Point out each Plasmodium parasite.
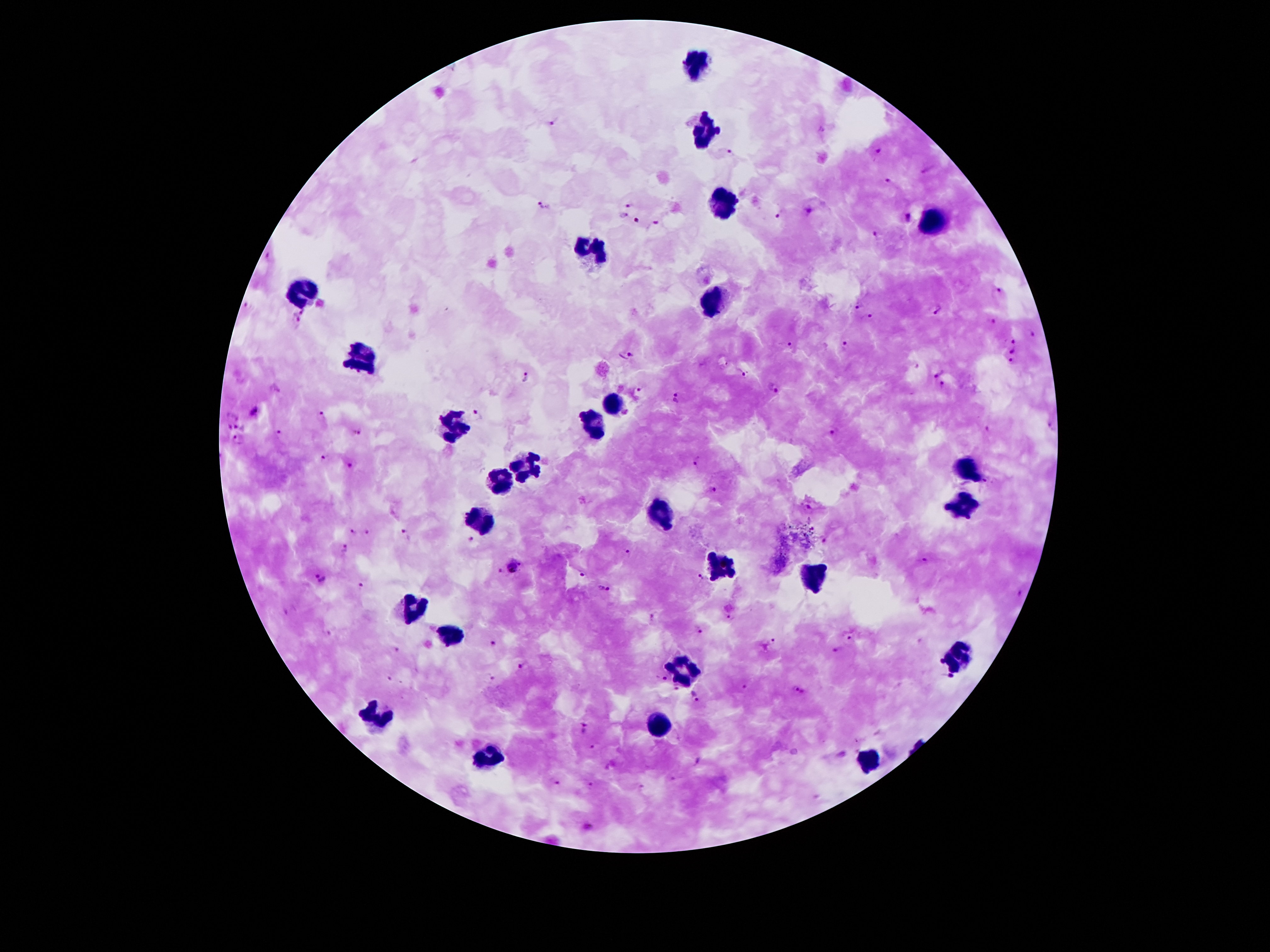

Approximate object centers, in pixels from the top-left corner.
Plasmodium parasites: (x=554, y=123), (x=879, y=153), (x=729, y=155), (x=887, y=179), (x=628, y=203), (x=543, y=207), (x=809, y=209), (x=780, y=213), (x=624, y=214), (x=908, y=218), (x=635, y=220), (x=657, y=221), (x=876, y=235), (x=267, y=257), (x=998, y=292), (x=246, y=304), (x=858, y=307), (x=303, y=310), (x=938, y=310), (x=872, y=315), (x=297, y=319), (x=992, y=320), (x=1032, y=335), (x=1013, y=342), (x=846, y=343), (x=791, y=344), (x=1012, y=352), (x=628, y=354), (x=1012, y=361), (x=939, y=373), (x=747, y=375), (x=525, y=378), (x=943, y=385), (x=773, y=387), (x=276, y=388), (x=637, y=394), (x=679, y=399), (x=253, y=411), (x=478, y=414), (x=320, y=415), (x=229, y=425), (x=237, y=426), (x=1051, y=427), (x=986, y=428), (x=354, y=431), (x=835, y=431), (x=278, y=433), (x=236, y=439), (x=321, y=456), (x=697, y=460), (x=348, y=468), (x=711, y=490), (x=352, y=531), (x=366, y=531), (x=406, y=534), (x=471, y=538), (x=825, y=541), (x=347, y=548), (x=628, y=551), (x=923, y=560), (x=520, y=564), (x=510, y=566), (x=499, y=570), (x=583, y=574), (x=700, y=576), (x=321, y=577), (x=361, y=586), (x=604, y=588), (x=1020, y=591), (x=731, y=618), (x=653, y=619), (x=699, y=629), (x=328, y=632), (x=849, y=638), (x=771, y=641), (x=494, y=643), (x=838, y=648), (x=397, y=649), (x=942, y=661), (x=522, y=666), (x=389, y=677), (x=491, y=677), (x=663, y=677), (x=951, y=677), (x=745, y=686), (x=675, y=687), (x=795, y=688), (x=695, y=695), (x=586, y=728), (x=593, y=747), (x=698, y=761), (x=673, y=778), (x=554, y=781), (x=591, y=785), (x=586, y=828).

Summary:
  - Leukocyte locations: (x=698, y=63), (x=705, y=132), (x=721, y=204), (x=935, y=225), (x=598, y=248), (x=304, y=288), (x=717, y=296), (x=362, y=351), (x=616, y=401), (x=457, y=429), (x=595, y=429), (x=530, y=464), (x=971, y=470), (x=501, y=477), (x=961, y=504), (x=659, y=512), (x=486, y=519), (x=716, y=563), (x=816, y=578), (x=413, y=607), (x=449, y=630), (x=959, y=653), (x=684, y=660), (x=379, y=716), (x=660, y=725), (x=491, y=756), (x=864, y=758)
  - Capture: smartphone through the microscope eyepiece
  - Image size: 1270×952 pixels
  - Preparation: thick blood film
  - Patient malaria status: infected with Plasmodium falciparum
  - Stain: Giemsa
  - Magnification: 100x
  - Field of view: one from this slide